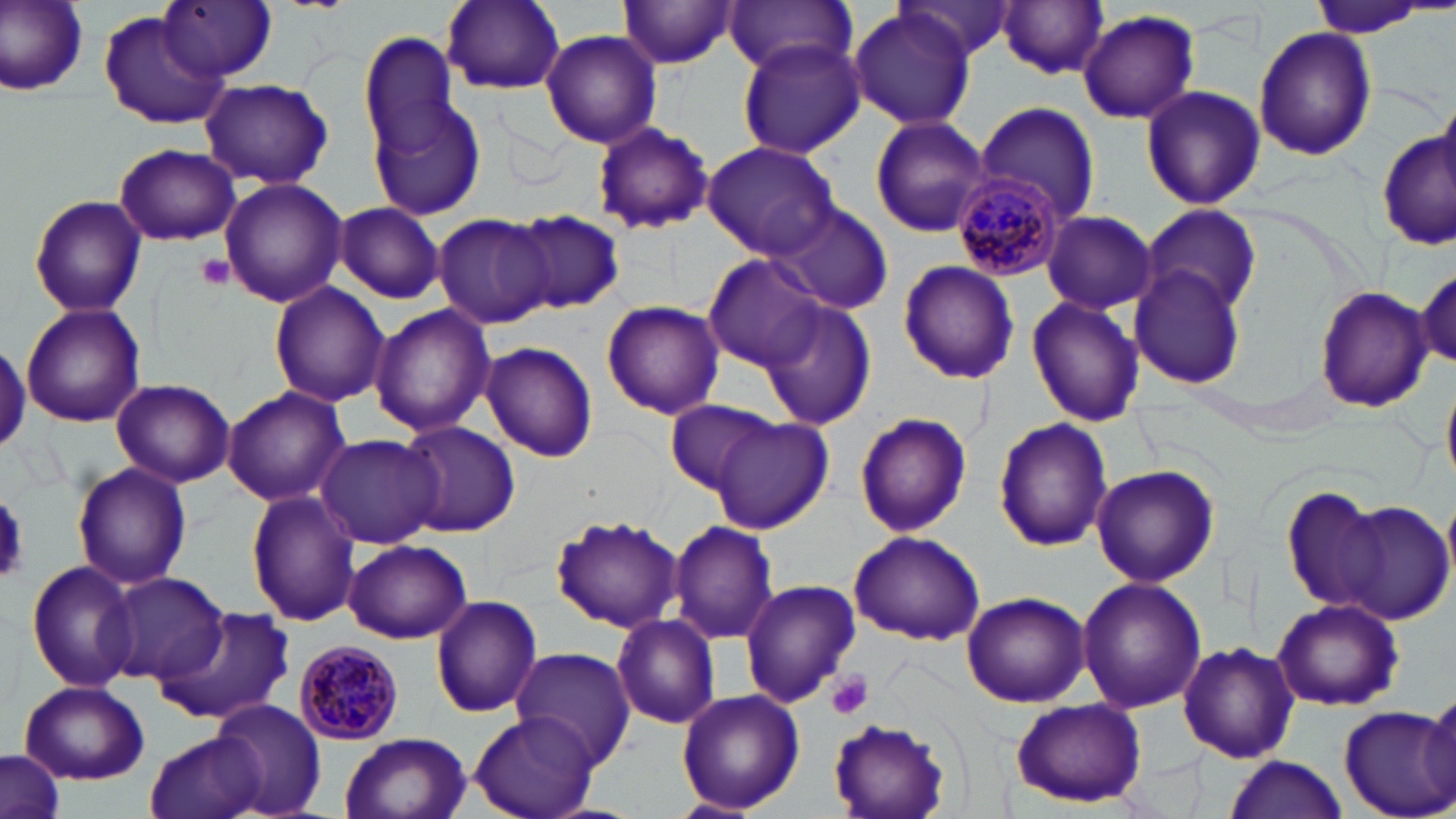
Summary:
  - Coordinate format: approximate bounding boxes as (x1, y1, x2, y2) in pixels
  - Plasmodium malariae-infected red blood cell locations: (950, 171, 1068, 279), (294, 640, 404, 745)
  - Uninfected red blood cell locations: (2, 0, 91, 96), (160, 0, 277, 81), (441, 0, 566, 93), (722, 0, 857, 75), (893, 0, 1018, 65), (617, 1, 739, 69), (998, 1, 1110, 79), (1305, 1, 1436, 39), (847, 10, 976, 131), (100, 11, 228, 129), (1077, 11, 1199, 124), (1253, 25, 1377, 160), (539, 29, 663, 148), (360, 31, 463, 158), (736, 37, 865, 159), (199, 77, 334, 189), (1140, 85, 1265, 210), (370, 95, 488, 222), (975, 102, 1100, 222), (869, 115, 992, 237), (592, 121, 714, 235), (1378, 130, 1456, 253), (701, 139, 842, 260), (113, 142, 240, 247), (219, 175, 346, 308), (29, 194, 148, 318), (765, 200, 895, 313), (334, 202, 444, 303), (1141, 204, 1261, 314), (510, 210, 625, 314), (1041, 211, 1157, 314), (434, 212, 555, 329), (703, 253, 828, 370), (896, 261, 1020, 386), (1128, 265, 1249, 390), (1414, 265, 1455, 369), (267, 281, 389, 409), (1314, 285, 1432, 413), (1026, 296, 1143, 427), (758, 298, 877, 431), (601, 300, 725, 419), (21, 304, 146, 429), (368, 304, 495, 437), (480, 341, 599, 462), (1441, 375, 1456, 495), (111, 378, 235, 488), (221, 386, 350, 507), (664, 400, 781, 495), (853, 411, 974, 539), (708, 414, 833, 533), (993, 418, 1111, 552), (397, 421, 520, 538), (315, 433, 445, 550), (72, 462, 192, 591), (1091, 464, 1218, 587), (1280, 486, 1387, 615), (246, 490, 361, 628), (1330, 500, 1454, 625), (552, 513, 683, 633), (667, 519, 778, 646), (849, 531, 986, 646), (343, 539, 475, 642), (27, 560, 141, 694), (104, 572, 230, 685), (1076, 575, 1206, 715), (740, 579, 862, 706), (962, 592, 1090, 708), (430, 595, 544, 719), (1273, 598, 1402, 710), (153, 607, 295, 727), (610, 614, 722, 729), (1177, 641, 1301, 764), (511, 648, 635, 767), (18, 680, 149, 785), (676, 688, 805, 813), (1424, 689, 1455, 800), (1010, 698, 1147, 807), (211, 699, 327, 817), (1338, 705, 1456, 819), (469, 712, 601, 819), (827, 714, 954, 819), (146, 729, 263, 819), (339, 733, 471, 819), (1, 749, 65, 819), (1225, 755, 1348, 818)
  - Platelet locations: (196, 254, 234, 289), (0, 492, 25, 585), (826, 669, 874, 721)
  - Slide-level diagnosis: Plasmodium malariae
  - Field of view: one of a larger specimen
  - Modality: light microscopy
  - Magnification: 1000x
  - Stain: May-Grünwald-Giemsa
  - Preparation: thin blood smear
  - Image size: 1456×819 pixels